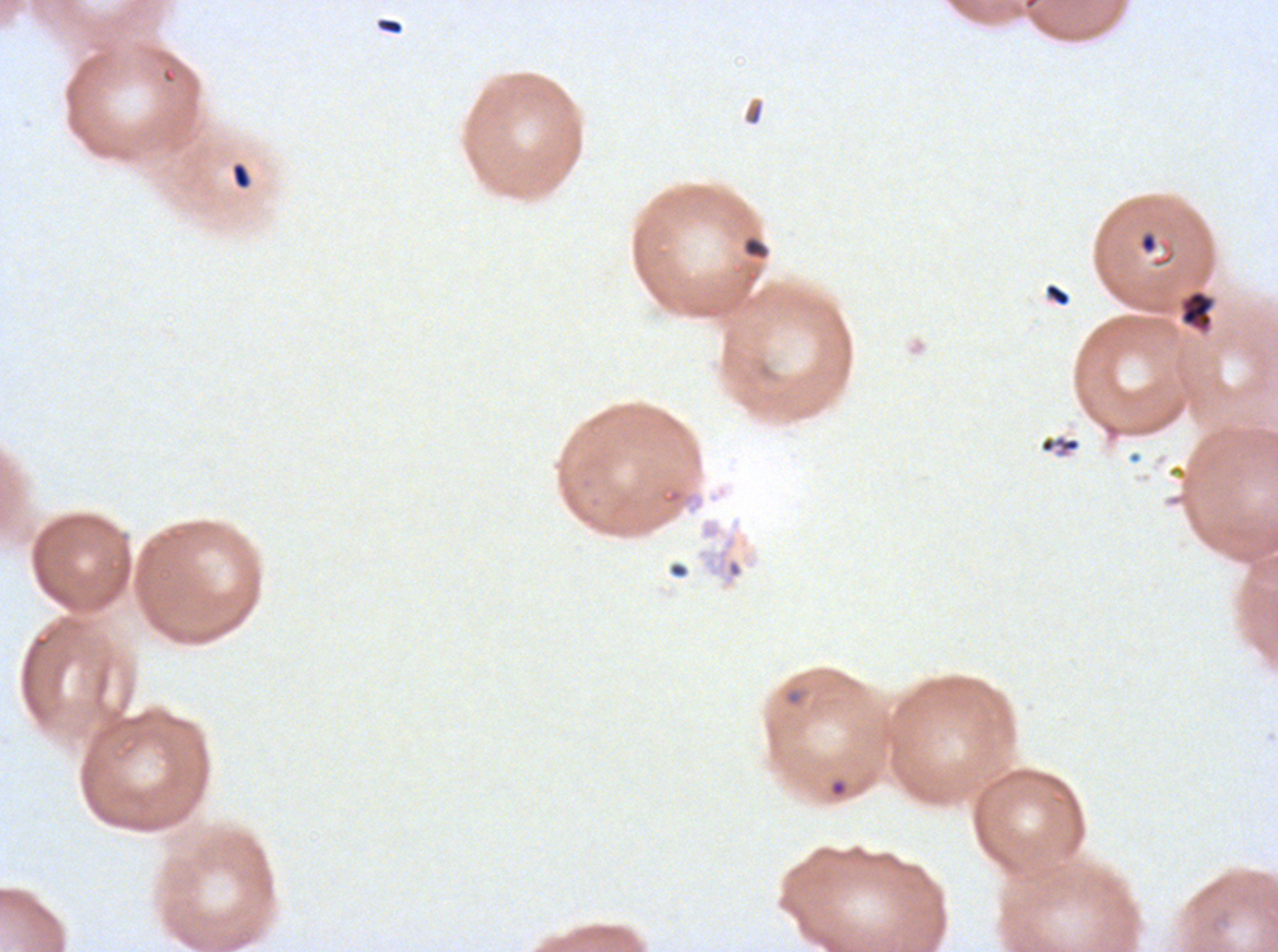

notation = approximate bounding boxes as {x1, y1, x2, y2} in pixels
debris locations = {379, 18, 403, 35}, {230, 162, 252, 190}, {1139, 232, 1158, 254}, {743, 236, 768, 260}, {1044, 283, 1071, 307}, {1180, 290, 1214, 332}, {1038, 433, 1081, 457}
ring locations = {784, 689, 804, 706}, {829, 778, 848, 798}
specimen = ex-vivo P. falciparum culture from a patient in The Gambia, grown for 24 to 48 hours
field of view = one sub-image of a larger composite
preparation = thin blood smear
image size = 1278×952 pixels
stain = Giemsa